Report the malaria status of this cell.
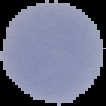

Parasitized.

Summary:
  - Preparation: thin blood smear
  - Image type: segmented cell region with the area outside set to black
  - Image size: 106×106 pixels